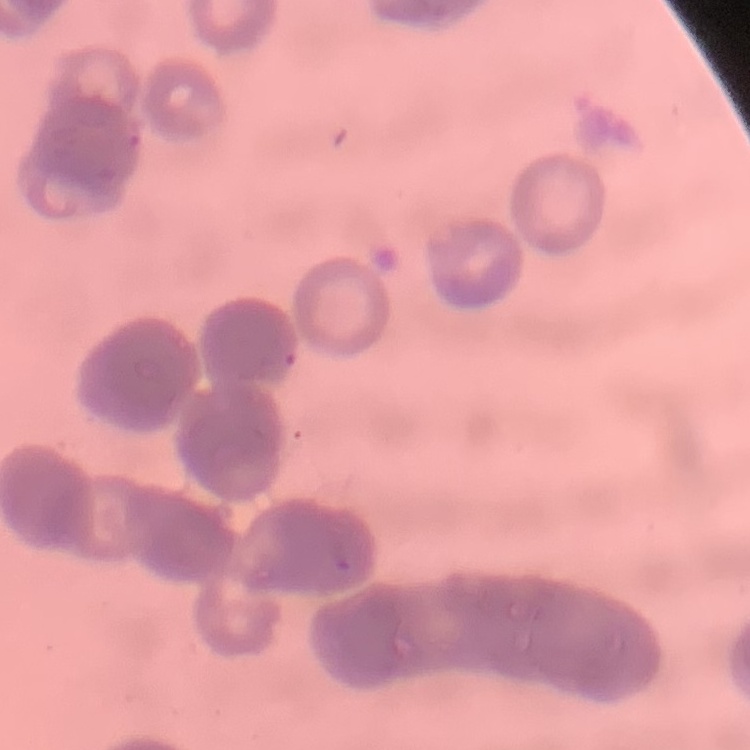

Summary:
  - Red blood cell morphology: rouleaux formation
  - Image type: one tile cut from a larger photomicrograph
  - Preparation: thin blood smear
  - Stain: Field's or Giemsa